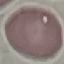

Malaria status: uninfected. Cell patch, automatically extracted from a larger field of view and resized to 64 × 64 pixels. Photographed with a smartphone camera at the microscope eyepiece. Thin smear of blood. Giemsa stain.